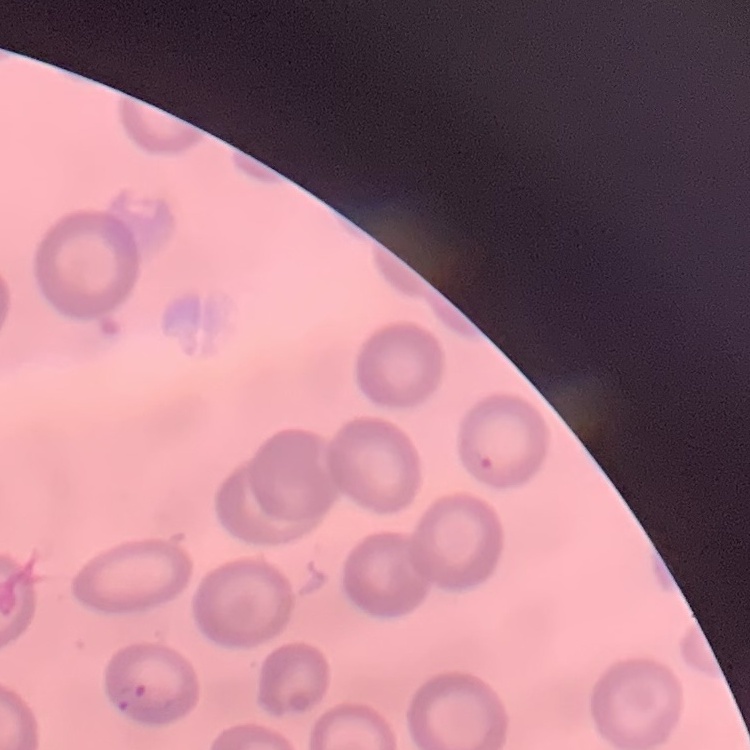
Summary:
  - Red blood cell morphology: no rouleaux formation
  - Preparation: thin blood smear
  - Stain: Field's or Giemsa
  - Image type: one tile cut from a larger photomicrograph